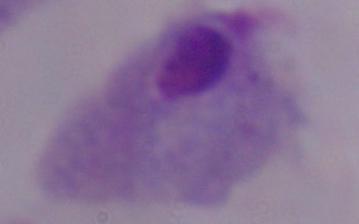

Summary:
  - Modality: micrograph
  - Identification: trichomonad
  - Magnification: 1000x